Assess this cell for malaria.
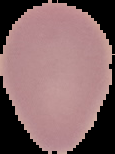

It is uninfected.

preparation: thin blood film
image_type: cell region segmented out of the field of view; surrounding area masked to black
image_size: 115×154 pixels